Give the position of every malaria parasite.
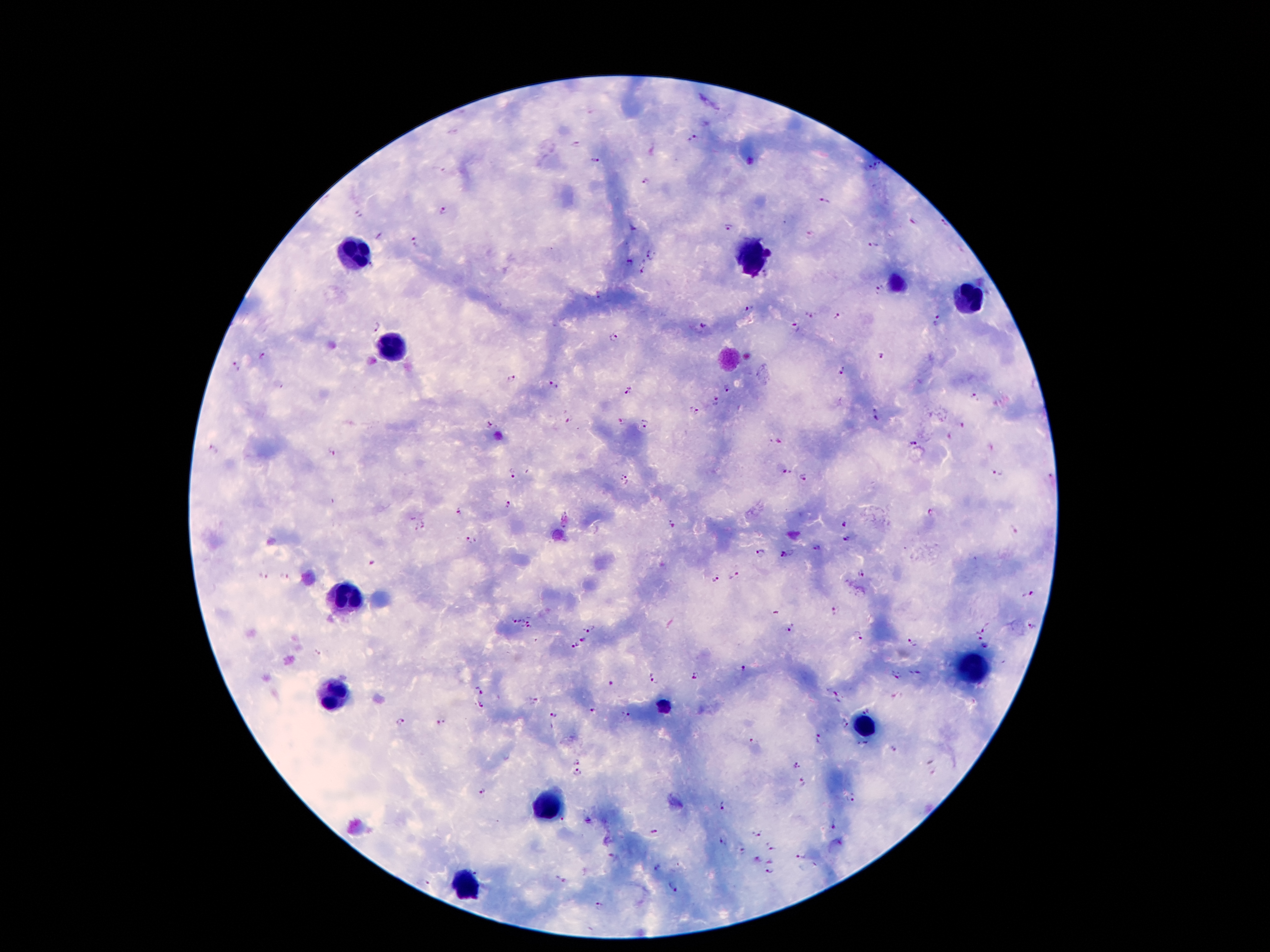

Approximate centers as (x, y) in pixels.
Malaria parasites: (694, 139), (576, 143), (595, 160), (879, 165), (867, 168), (438, 171), (646, 181), (825, 200), (445, 209), (356, 214), (945, 224), (728, 226), (634, 228), (809, 234), (415, 241), (872, 246), (652, 255), (628, 262), (372, 267), (641, 271), (878, 292), (598, 296), (749, 307), (811, 315), (837, 316), (938, 320), (374, 327), (704, 327), (795, 328), (614, 337), (263, 356), (882, 357), (237, 367), (843, 369), (511, 379), (555, 385), (629, 388), (726, 388), (973, 397), (716, 400), (694, 411), (876, 414), (568, 421), (622, 421), (489, 424), (644, 425), (963, 427), (781, 442), (914, 443), (214, 448), (334, 451), (787, 471), (997, 471), (510, 473), (1050, 476), (805, 477), (623, 480), (508, 506), (457, 509), (931, 513), (671, 523), (845, 523), (1013, 530), (471, 540), (846, 540), (818, 549), (759, 554), (784, 555), (371, 565), (863, 572), (263, 575), (285, 576), (733, 576), (714, 579), (1028, 594), (835, 610), (528, 617), (516, 620), (589, 627), (790, 628), (987, 628), (1033, 628), (527, 629), (977, 637), (859, 638), (585, 640), (914, 642), (576, 645), (318, 654), (745, 669), (916, 672), (896, 674), (697, 676), (652, 679), (611, 682), (477, 687), (836, 696), (533, 699), (480, 704), (590, 711), (555, 714), (626, 715), (401, 723), (439, 724), (821, 737), (753, 740), (576, 761), (795, 764), (578, 774), (801, 780), (481, 791), (851, 798), (725, 806), (832, 830), (756, 833), (655, 834), (721, 841), (770, 846), (743, 852), (801, 856), (758, 861), (658, 869), (770, 873), (559, 880), (424, 882), (671, 888), (599, 905).

leukocyte locations = (356, 254), (751, 259), (965, 306), (391, 345), (347, 597), (972, 665), (333, 700), (863, 730), (548, 807), (468, 882)
stain = Giemsa
patient malaria status = positive for Plasmodium falciparum
preparation = thick blood smear
field of view = one from this slide
image size = 1270×952 pixels
magnification = 100x
capture = smartphone through the microscope eyepiece